Name the parasite shown.
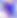
This is Toxoplasma gondii.

Summary:
  - Modality: photomicrograph
  - Magnification: 400x